Assess this cell for malaria.
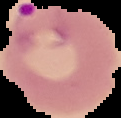
Parasitized.

{
  "preparation": "thin blood smear",
  "image_size": "121×118 pixels",
  "image_type": "segmented cell region on a black background"
}